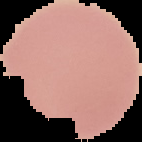

preparation = thin blood film
image size = 142×142 pixels
malaria status = uninfected
image type = cell region segmented out of the field of view; surrounding area masked to black